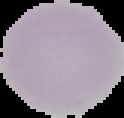

From a thin blood film. Malaria status: uninfected. The area outside the segmented cell region is set to black. Image is 124×118 pixels.